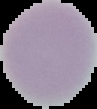 Result: no malaria parasites detected. From a thin blood smear. Segmented cell region on a black background. Image is 97×109 pixels.